Point out each leukocyte.
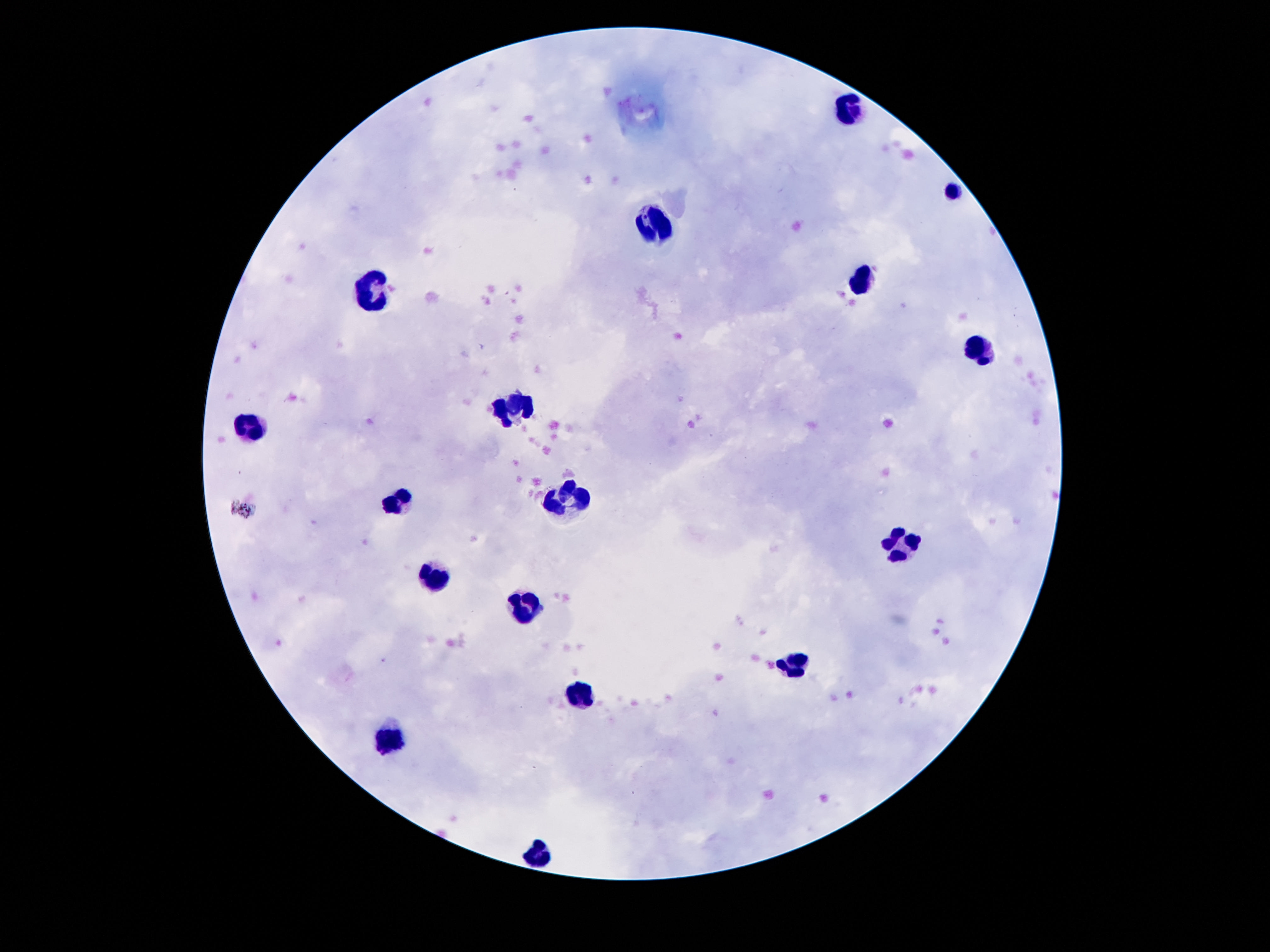
Approximate centers as {x, y} in pixels.
Leukocytes: {848, 110}, {652, 222}, {370, 285}, {858, 287}, {979, 351}, {517, 407}, {251, 428}, {561, 500}, {398, 502}, {900, 542}, {433, 568}, {526, 607}, {797, 663}, {580, 693}, {388, 744}, {540, 849}.

capture = smartphone camera through the microscope eyepiece
image size = 1270×952 pixels
magnification = 100x
field of view = one from this slide
patient malaria status = not infected
preparation = thick blood film
stain = Giemsa